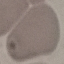
malaria_status: uninfected
preparation: thin blood smear
stain: Giemsa
image_type: cell patch, automatically extracted from a larger field of view and resized to 64 × 64 pixels
capture: smartphone camera at the microscope eyepiece